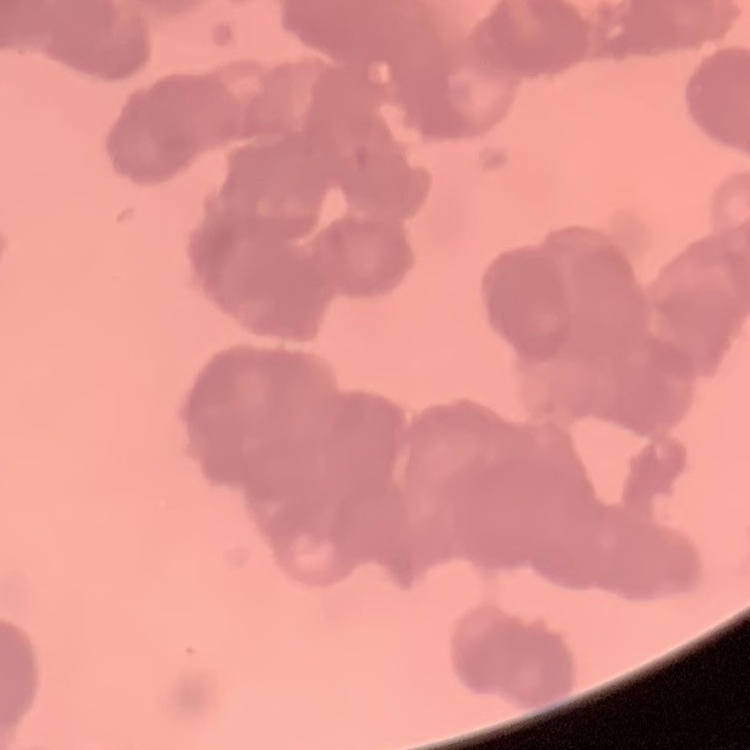

Summary:
  - Erythrocyte morphology: rouleaux formation
  - Stain: Field's or Giemsa
  - Preparation: thin blood smear
  - Image type: square crop of a larger photomicrograph